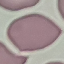 Result: negative for malaria parasites. Thin blood smear. Giemsa-stained preparation. Automatically extracted cell patch, resized to 64 × 64 pixels. Photographed with a smartphone camera at the microscope eyepiece.